Identify the parasite.
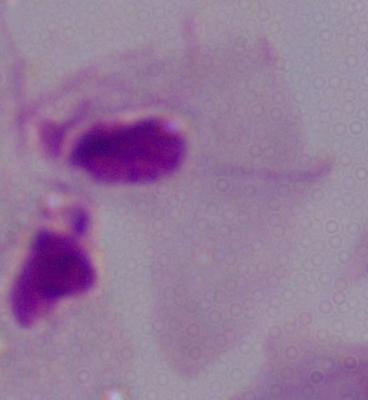

A trichomonad.

modality = micrograph
magnification = 1000x